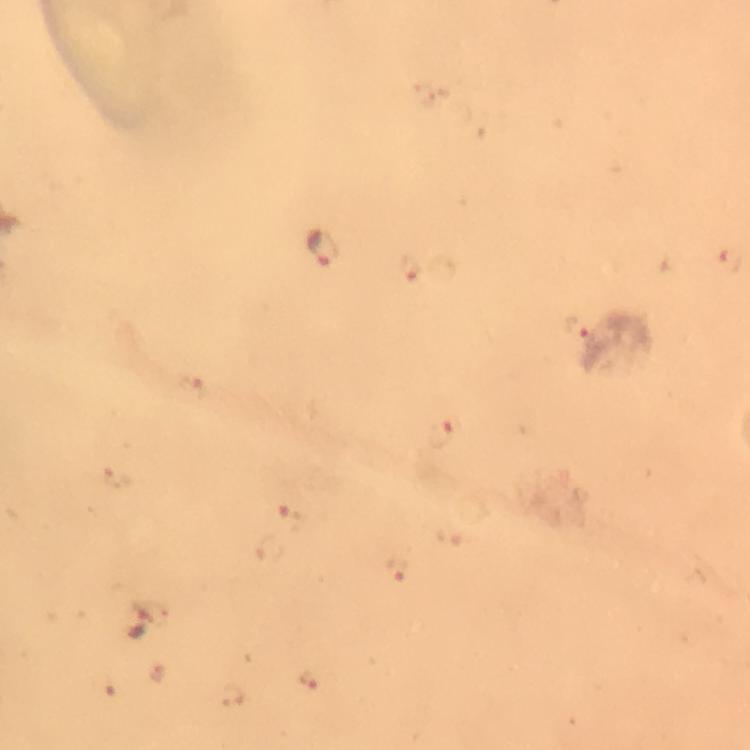

Approximate object centers, in pixels from the top-left corner. Malaria parasite locations: (x=325, y=249), (x=410, y=268), (x=576, y=328), (x=191, y=391), (x=443, y=433), (x=292, y=516), (x=398, y=570), (x=142, y=622), (x=159, y=671), (x=309, y=680), (x=232, y=697). Image is 750×750 pixels. Immersion oil applied. Thick blood film. A crop from one field of view. At 100x magnification. Photographed with a smartphone mounted on the microscope. From a diagnostic examination for malaria. Giemsa stain.